Name the parasite shown.
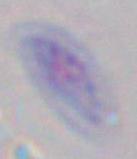

Toxoplasma gondii.

1000x magnification. Photomicrograph.